Classify this cell by malaria status.
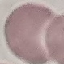

Uninfected.

Thin blood film. Acquired by smartphone through the microscope eyepiece. Cell patch, automatically extracted from a larger field of view and resized to 64 × 64 pixels. Giemsa-stained preparation.